Locate every Plasmodium falciparum-infected red blood cell.
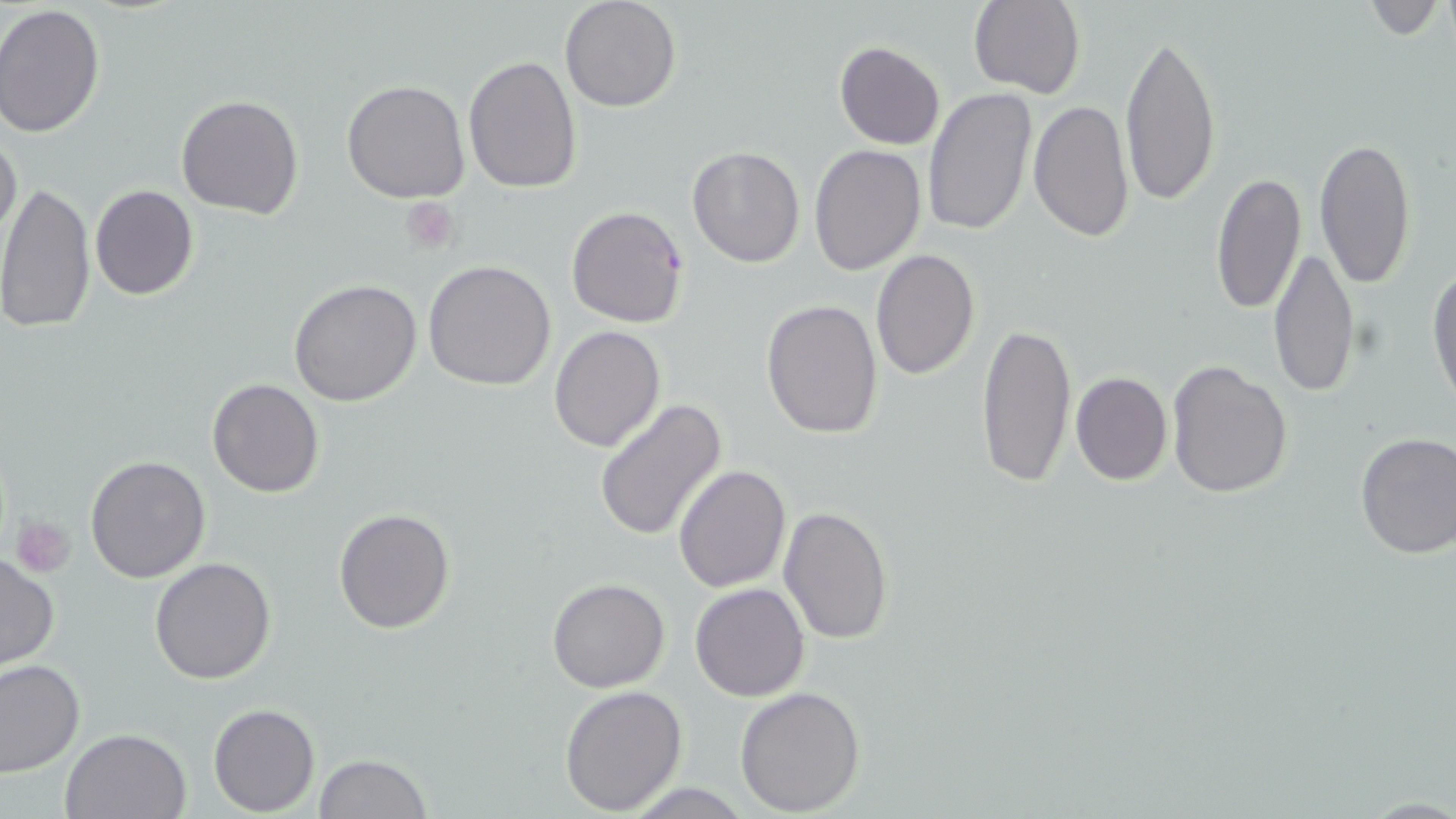

Approximate bounding boxes as named x1/y1/x2/y2 corners in pixels.
Plasmodium falciparum-infected red blood cells: (x1=566, y1=205, x2=690, y2=329).

Uninfected red blood cell locations: (x1=559, y1=0, x2=682, y2=112), (x1=969, y1=0, x2=1087, y2=100), (x1=1354, y1=2, x2=1449, y2=37), (x1=0, y1=5, x2=105, y2=139), (x1=1119, y1=29, x2=1222, y2=211), (x1=834, y1=41, x2=946, y2=150), (x1=464, y1=55, x2=581, y2=194), (x1=340, y1=80, x2=470, y2=203), (x1=922, y1=87, x2=1035, y2=239), (x1=175, y1=94, x2=303, y2=220), (x1=1028, y1=99, x2=1135, y2=241), (x1=0, y1=129, x2=22, y2=250), (x1=1314, y1=137, x2=1417, y2=289), (x1=809, y1=143, x2=927, y2=274), (x1=687, y1=145, x2=805, y2=268), (x1=1210, y1=172, x2=1306, y2=316), (x1=0, y1=180, x2=97, y2=335), (x1=91, y1=184, x2=197, y2=300), (x1=1268, y1=246, x2=1361, y2=399), (x1=869, y1=249, x2=980, y2=379), (x1=423, y1=259, x2=556, y2=391), (x1=1427, y1=260, x2=1456, y2=415), (x1=289, y1=280, x2=422, y2=406), (x1=761, y1=299, x2=884, y2=440), (x1=975, y1=318, x2=1076, y2=489), (x1=549, y1=325, x2=666, y2=451), (x1=1167, y1=361, x2=1293, y2=501), (x1=1070, y1=372, x2=1172, y2=486), (x1=207, y1=378, x2=324, y2=497), (x1=594, y1=400, x2=727, y2=542), (x1=1355, y1=432, x2=1455, y2=559), (x1=85, y1=454, x2=211, y2=583), (x1=675, y1=464, x2=791, y2=593), (x1=777, y1=504, x2=893, y2=645), (x1=334, y1=506, x2=456, y2=632), (x1=1, y1=552, x2=59, y2=669), (x1=150, y1=557, x2=276, y2=685), (x1=547, y1=577, x2=670, y2=693), (x1=691, y1=583, x2=809, y2=701), (x1=0, y1=659, x2=84, y2=775), (x1=559, y1=683, x2=687, y2=815), (x1=735, y1=685, x2=865, y2=815), (x1=208, y1=703, x2=319, y2=815), (x1=61, y1=728, x2=190, y2=818), (x1=314, y1=754, x2=434, y2=818). Platelet locations: (x1=402, y1=199, x2=460, y2=252), (x1=12, y1=515, x2=74, y2=576). Slide-level diagnosis: Plasmodium falciparum. One field of a larger specimen. Thin blood film. Image is 1456×819 pixels. Light microscopy. Captured at 1000x magnification. May-Grünwald-Giemsa stain.